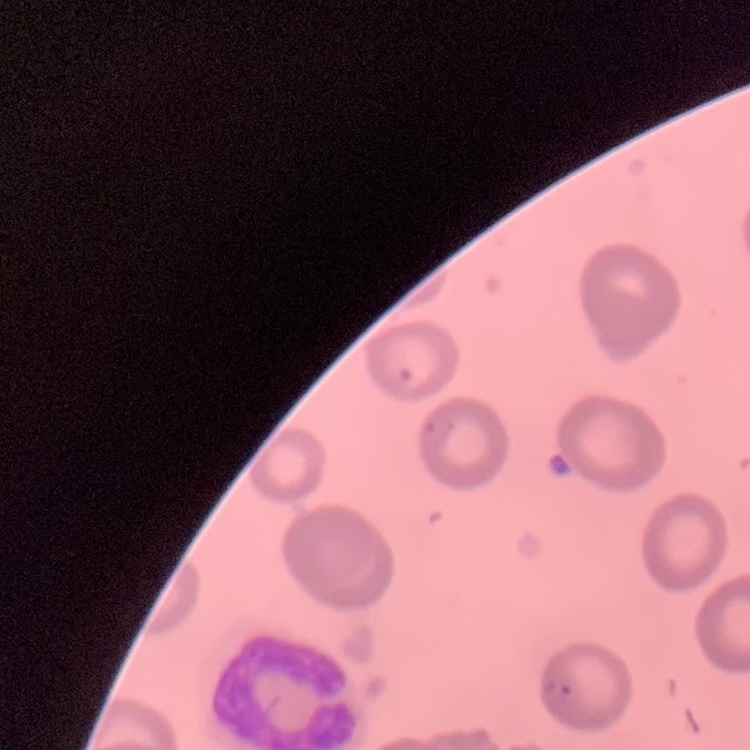
red blood cell morphology = no rouleaux formation
stain = Field's or Giemsa
image type = one tile cut from a larger photomicrograph
preparation = thin blood smear